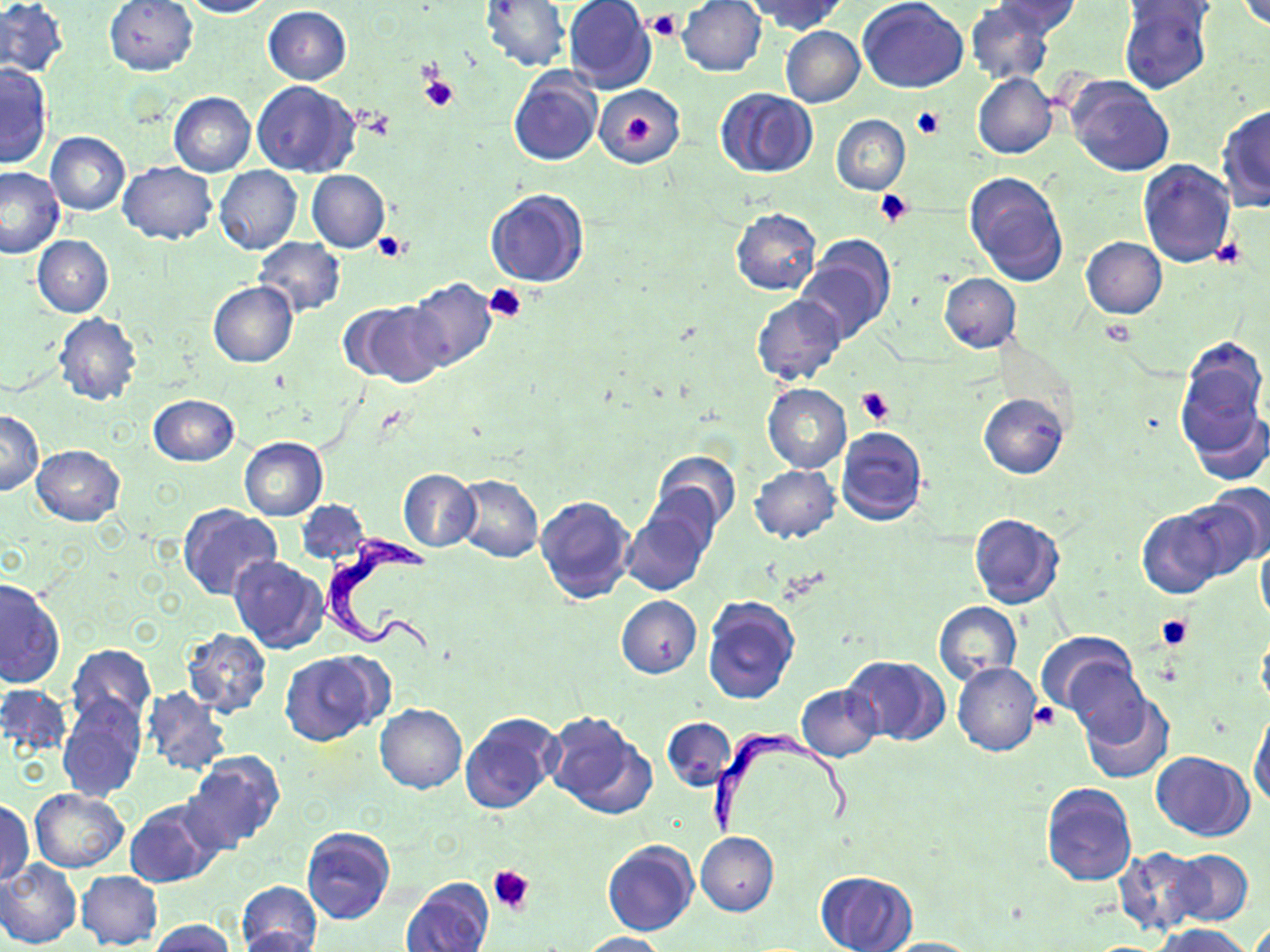
Summary:
  - Coordinate format: approximate bounding boxes as [x1, y1, x2, y2] in pixels
  - Uninfected red blood cell locations: [104, 0, 199, 75], [180, 0, 274, 18], [481, 0, 570, 72], [564, 0, 656, 93], [677, 0, 767, 76], [749, 0, 846, 35], [858, 0, 969, 93], [994, 0, 1080, 37], [1235, 0, 1269, 31], [0, 1, 68, 78], [1118, 1, 1213, 94], [965, 2, 1055, 85], [1120, 3, 1219, 30], [263, 6, 351, 84], [779, 26, 865, 108], [1, 66, 52, 169], [509, 68, 603, 166], [972, 73, 1058, 159], [1065, 73, 1175, 177], [252, 81, 360, 177], [594, 85, 685, 168], [715, 87, 817, 177], [168, 92, 255, 177], [1216, 103, 1270, 211], [831, 114, 909, 195], [45, 131, 130, 215], [1138, 160, 1235, 267], [118, 162, 218, 244], [0, 166, 66, 259], [214, 166, 302, 255], [307, 170, 389, 252], [964, 170, 1068, 285], [484, 188, 588, 287], [730, 209, 822, 295], [33, 235, 114, 317], [252, 237, 345, 316], [797, 237, 895, 343], [1080, 237, 1167, 319], [939, 273, 1021, 352], [405, 278, 498, 373], [208, 280, 297, 367], [752, 294, 847, 385], [343, 301, 445, 388], [55, 313, 141, 406], [1175, 345, 1269, 475], [763, 383, 851, 473], [979, 392, 1069, 479], [147, 395, 238, 467], [1189, 404, 1269, 486], [0, 411, 43, 495], [835, 427, 927, 528], [240, 437, 327, 520], [31, 444, 125, 525], [652, 450, 741, 535], [750, 465, 841, 543], [398, 469, 479, 552], [637, 471, 728, 563], [455, 475, 544, 563], [1173, 491, 1269, 582], [535, 494, 634, 603], [296, 499, 371, 567], [179, 504, 281, 599], [620, 505, 713, 598], [1136, 507, 1226, 598], [970, 512, 1065, 609], [1256, 535, 1270, 630], [229, 556, 330, 655], [0, 577, 64, 688], [616, 595, 702, 678], [701, 595, 800, 705], [933, 601, 1022, 683], [181, 627, 272, 717], [1257, 627, 1270, 715], [1039, 631, 1139, 721], [67, 643, 155, 726], [279, 650, 388, 745], [843, 654, 950, 747], [1064, 654, 1153, 745], [952, 662, 1041, 755], [0, 685, 72, 758], [141, 686, 230, 776], [795, 686, 881, 762], [1077, 691, 1173, 784], [57, 693, 145, 800], [375, 704, 466, 793], [1249, 708, 1270, 810], [542, 710, 655, 817], [459, 712, 563, 812], [662, 717, 736, 793], [183, 751, 285, 851], [1150, 751, 1255, 841], [1041, 782, 1137, 886], [29, 788, 129, 872], [0, 799, 33, 887], [125, 801, 223, 887], [302, 826, 395, 924], [696, 831, 778, 917], [602, 840, 698, 936], [1115, 846, 1206, 934], [1169, 850, 1253, 926], [243, 857, 392, 949], [0, 860, 82, 949], [77, 870, 163, 950], [817, 870, 915, 952], [401, 877, 494, 952], [236, 881, 323, 952], [150, 919, 235, 952], [1151, 924, 1254, 952], [235, 927, 323, 952], [578, 931, 668, 952], [877, 937, 984, 951]
  - Trypanosoma brucei locations: [320, 533, 443, 662], [707, 730, 858, 836]
  - Platelet locations: [647, 10, 681, 41], [419, 70, 455, 110], [912, 106, 944, 139], [622, 115, 657, 146], [874, 188, 913, 227], [373, 233, 410, 264], [1211, 236, 1245, 268], [485, 283, 528, 324], [1100, 318, 1137, 347], [858, 388, 895, 426], [1155, 612, 1194, 651], [1030, 704, 1056, 728], [489, 864, 533, 913]
  - Slide-level diagnosis: Trypanosoma brucei
  - Preparation: thin blood film
  - Stain: May-Grünwald-Giemsa
  - Magnification: 1000x
  - Image size: 1270×952 pixels
  - Field of view: single
  - Modality: light microscopy